Identify the preparation type.
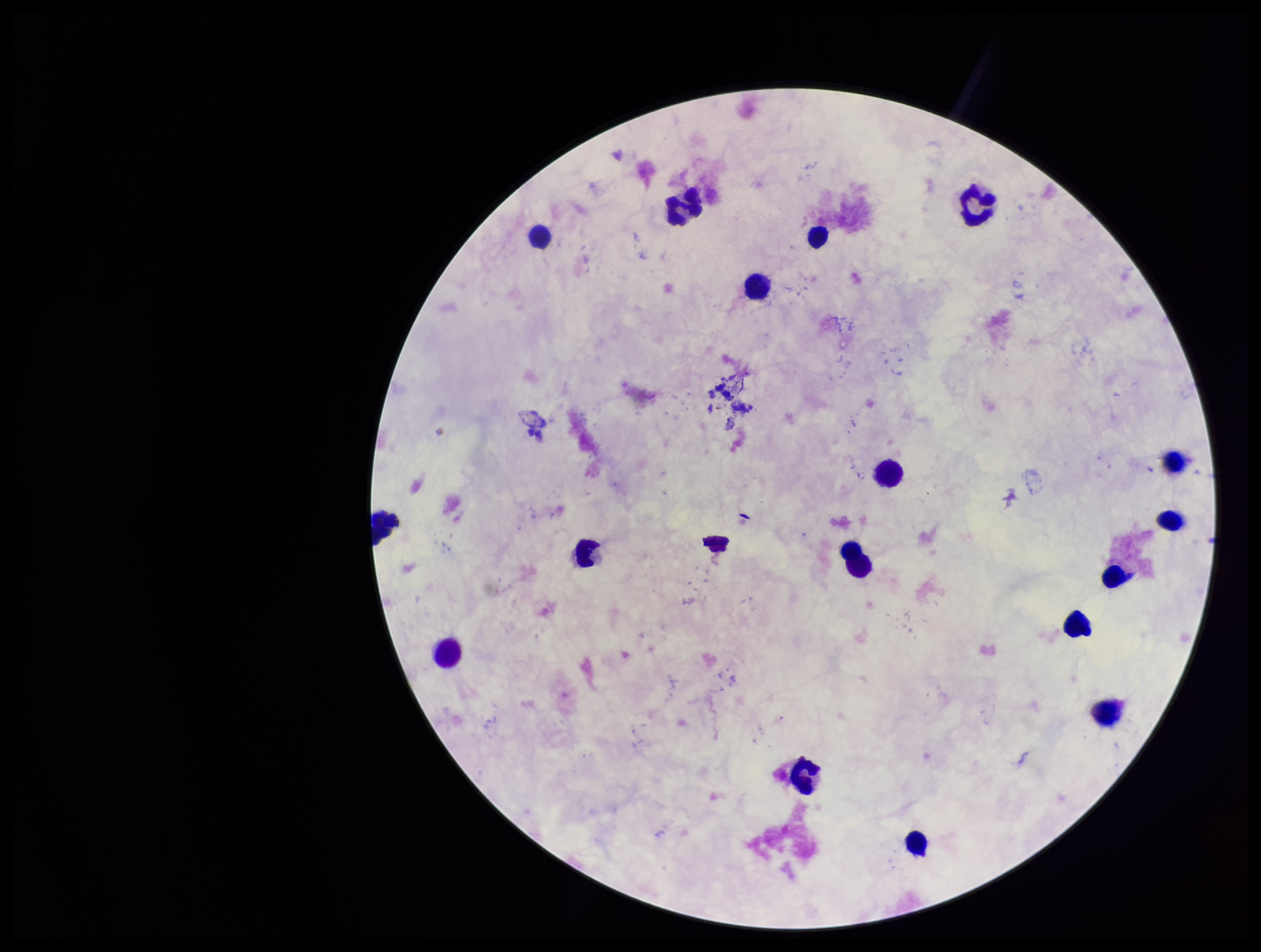
A thick smear.

Parasite count: 0. Plasmodium parasites: none identified. Image is 1261×952 pixels. Photographed through the microscope eyepiece with a smartphone camera. Patient malaria status: negative. Leukocyte count: 17. Single field of view. Giemsa stain.